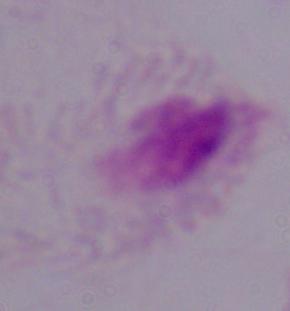 A trichomonad is shown. 1000x magnification. Micrograph.